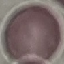

Result: negative for malaria parasites. Photographed with a smartphone camera at the microscope eyepiece. Automatically extracted cell patch, resized to 64 × 64 pixels. Giemsa-stained preparation. Thin blood film.